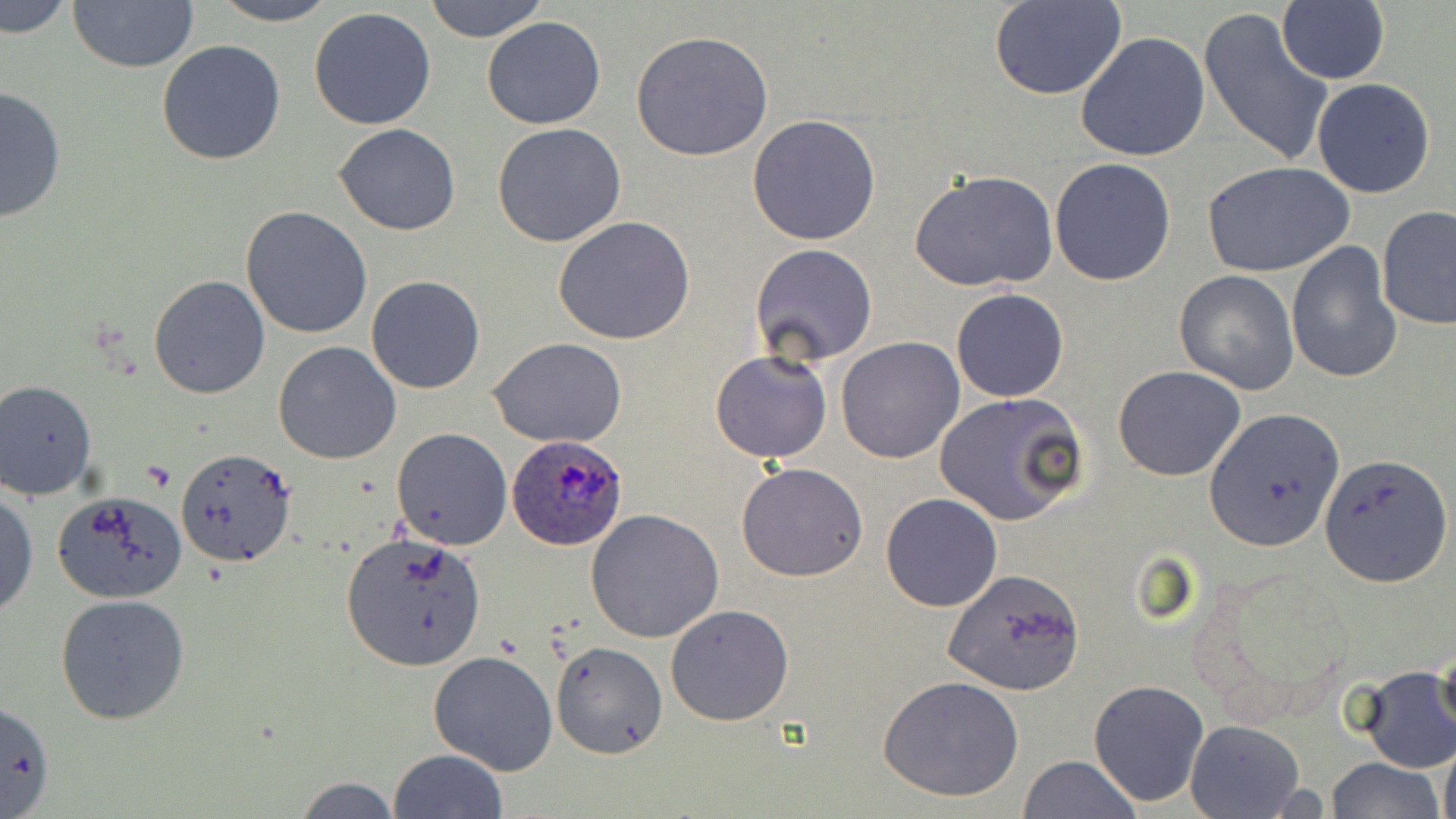

Summary:
  - Coordinate format: approximate bounding boxes as named x1/y1/x2/y2 corners in pixels
  - Plasmodium ovale-infected red blood cell locations: (x1=505, y1=436, x2=628, y2=551)
  - Uninfected red blood cell locations: (x1=0, y1=0, x2=74, y2=40), (x1=207, y1=0, x2=341, y2=26), (x1=424, y1=0, x2=549, y2=43), (x1=990, y1=1, x2=1127, y2=100), (x1=68, y1=2, x2=199, y2=74), (x1=1278, y1=3, x2=1389, y2=84), (x1=308, y1=8, x2=438, y2=130), (x1=1199, y1=9, x2=1335, y2=167), (x1=482, y1=16, x2=605, y2=129), (x1=629, y1=30, x2=775, y2=160), (x1=1076, y1=31, x2=1210, y2=161), (x1=156, y1=40, x2=287, y2=166), (x1=1312, y1=77, x2=1437, y2=199), (x1=0, y1=84, x2=70, y2=223), (x1=748, y1=114, x2=881, y2=246), (x1=492, y1=123, x2=625, y2=248), (x1=334, y1=124, x2=460, y2=234), (x1=1049, y1=157, x2=1177, y2=287), (x1=1201, y1=160, x2=1354, y2=277), (x1=909, y1=169, x2=1059, y2=290), (x1=241, y1=206, x2=372, y2=339), (x1=1378, y1=206, x2=1456, y2=330), (x1=552, y1=216, x2=696, y2=345), (x1=1285, y1=238, x2=1400, y2=383), (x1=749, y1=244, x2=878, y2=366), (x1=1174, y1=269, x2=1301, y2=395), (x1=148, y1=274, x2=270, y2=399), (x1=366, y1=276, x2=485, y2=394), (x1=951, y1=288, x2=1069, y2=403), (x1=488, y1=337, x2=628, y2=448), (x1=836, y1=338, x2=966, y2=463), (x1=273, y1=341, x2=401, y2=464), (x1=710, y1=349, x2=833, y2=462), (x1=1114, y1=366, x2=1245, y2=481), (x1=0, y1=380, x2=97, y2=500), (x1=934, y1=391, x2=1089, y2=526), (x1=1206, y1=409, x2=1342, y2=550), (x1=391, y1=428, x2=512, y2=549), (x1=176, y1=448, x2=296, y2=568), (x1=1321, y1=454, x2=1451, y2=583), (x1=736, y1=462, x2=869, y2=582), (x1=0, y1=487, x2=38, y2=618), (x1=53, y1=489, x2=190, y2=603), (x1=880, y1=491, x2=1002, y2=612), (x1=584, y1=509, x2=725, y2=643), (x1=341, y1=535, x2=488, y2=672), (x1=942, y1=568, x2=1087, y2=696), (x1=55, y1=594, x2=189, y2=725), (x1=665, y1=603, x2=796, y2=725), (x1=551, y1=641, x2=669, y2=760), (x1=1432, y1=642, x2=1455, y2=741), (x1=429, y1=649, x2=559, y2=775), (x1=1354, y1=669, x2=1456, y2=773), (x1=879, y1=675, x2=1026, y2=803), (x1=1088, y1=679, x2=1211, y2=807), (x1=1, y1=700, x2=55, y2=819), (x1=1185, y1=720, x2=1306, y2=818), (x1=1439, y1=743, x2=1456, y2=819), (x1=389, y1=748, x2=508, y2=819), (x1=1018, y1=756, x2=1140, y2=818), (x1=1327, y1=757, x2=1445, y2=819), (x1=293, y1=776, x2=402, y2=818)
  - Slide-level diagnosis: Plasmodium ovale
  - Field of view: one of a larger specimen
  - Magnification: 1000x
  - Modality: optical microscopy
  - Preparation: thin blood film
  - Stain: May-Grünwald-Giemsa
  - Image size: 1456×819 pixels